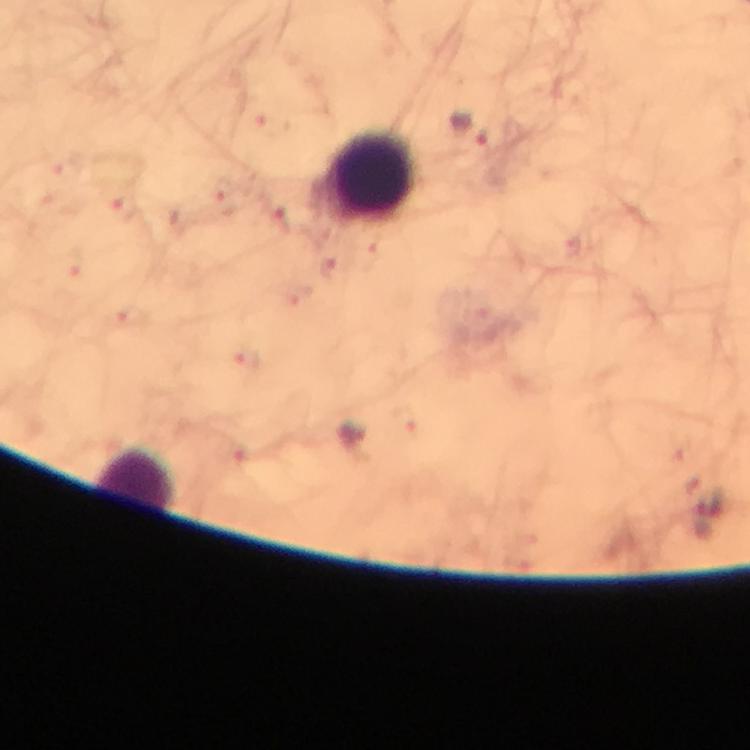
Approximate centers as (x, y) in pixels.
Summary:
  - Leukocyte locations: (373, 176), (135, 478)
  - Plasmodium parasite locations: (471, 127), (223, 188), (331, 265), (246, 360)
  - Image size: 750×750 pixels
  - Stain: Giemsa
  - Context: from a malaria diagnostic workup
  - Capture: smartphone camera through the microscope
  - Magnification: 100x
  - Immersion oil: applied
  - Preparation: thick blood smear
  - Cropped from: a single field of view